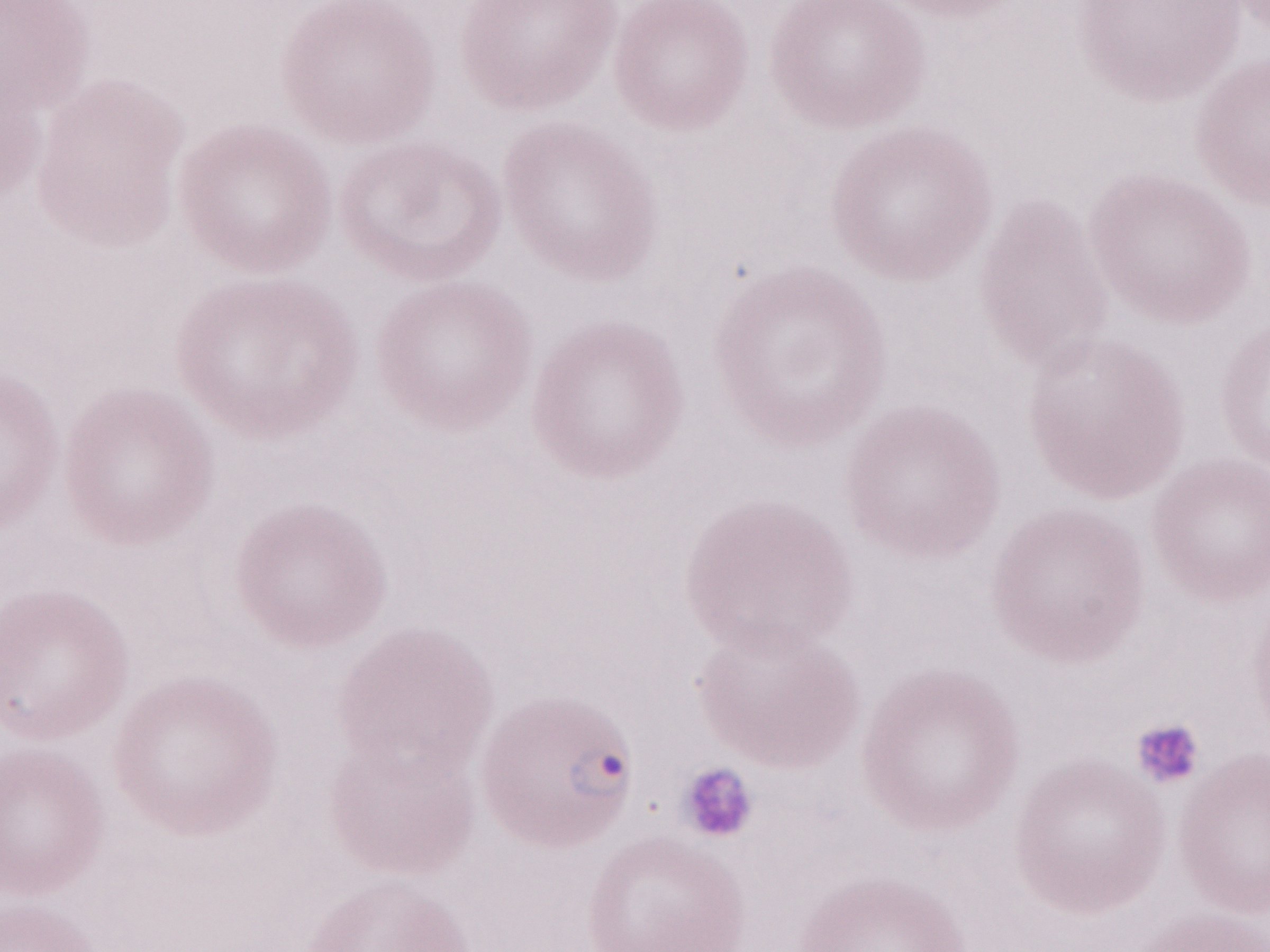

Thin blood smear. Malaria diagnosis (patient-level): positive. Image is 1270×952 pixels. Magnification: 1,000x. Single field of view. May-Grünwald-Giemsa stain. Olympus BX43 microscope and DP73 digital camera.